State which parasite is depicted.
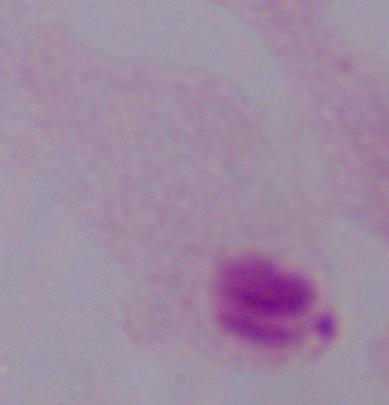

This is a trichomonad.

Summary:
  - Modality: photomicrograph
  - Magnification: 1000x